Locate every Plasmodium parasite.
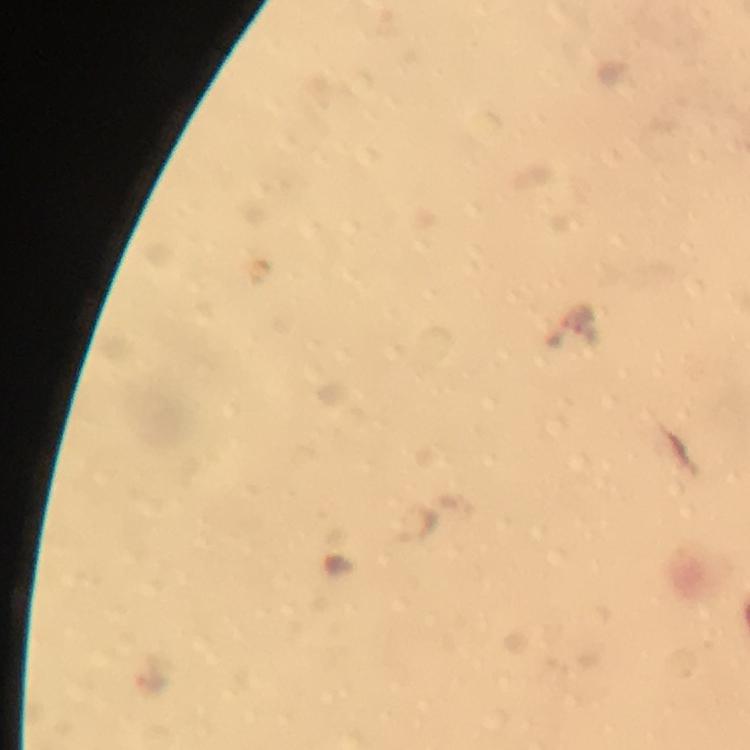

Approximate object centers, in pixels from the top-left corner.
Plasmodium parasites: (x=414, y=527).

Summary:
  - Magnification: 100x
  - Image size: 750×750 pixels
  - Preparation: thick smear
  - Cropped from: a single field of view
  - Immersion oil: applied
  - Stain: Giemsa
  - Context: from a malaria diagnostic workup
  - Capture: smartphone mounted on the microscope